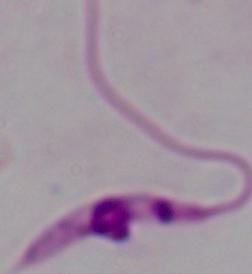
modality = micrograph
magnification = 1000x
identification = Leishmania